Locate and identify every blood parasite.
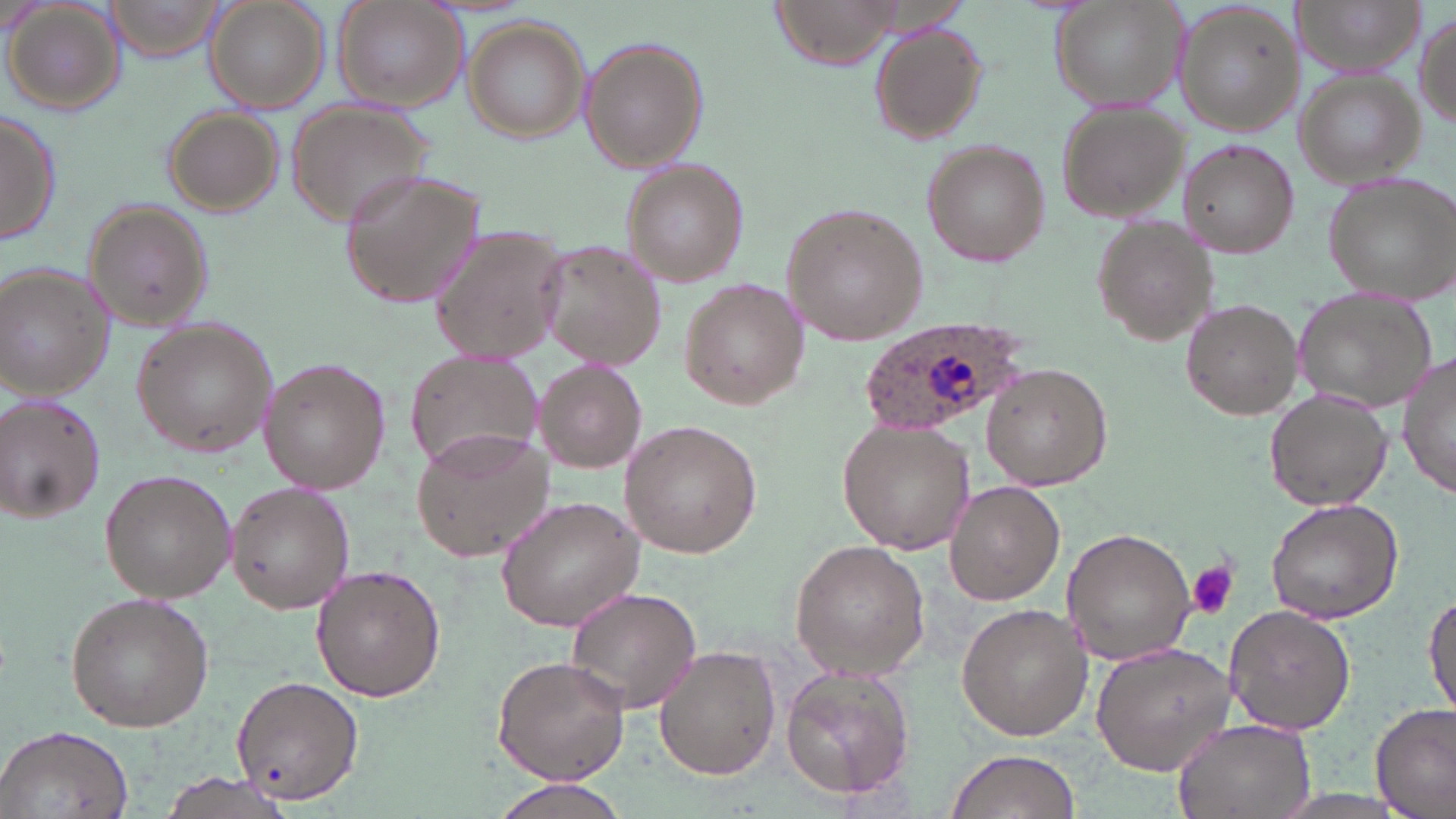

Approximate bounding boxes as (x1,y1)-(x2,y2) corner pairs in pixels.
Plasmodium ovale-infected red blood cells: (865,320)-(1031,440).
No Plasmodium falciparum, Plasmodium malariae, Plasmodium vivax, Babesia divergens, or Trypanosoma brucei observed.

Uninfected red blood cell locations: (202,0)-(332,113), (333,0)-(466,112), (770,0)-(908,71), (1051,0)-(1190,112), (1298,0)-(1421,73), (1174,2)-(1303,139), (4,4)-(125,114), (1414,11)-(1455,133), (464,17)-(590,145), (868,22)-(987,145), (581,36)-(708,175), (1294,70)-(1426,188), (288,102)-(433,229), (1056,104)-(1189,223), (161,107)-(286,219), (0,109)-(61,246), (923,141)-(1050,267), (1179,141)-(1299,258), (622,161)-(747,284), (340,168)-(486,312), (1323,173)-(1456,305), (86,204)-(215,332), (783,205)-(928,345), (1091,216)-(1215,349), (429,223)-(572,365), (539,243)-(668,370), (1,264)-(114,401), (679,279)-(807,409), (1296,290)-(1437,414), (1183,299)-(1304,420), (131,318)-(279,457), (1398,345)-(1455,502), (405,356)-(545,479), (259,359)-(390,495), (535,359)-(648,472), (983,363)-(1111,489), (1265,389)-(1394,511), (0,394)-(107,524), (622,420)-(763,556), (839,420)-(974,552), (412,425)-(555,562), (100,468)-(237,603), (225,480)-(354,614), (943,480)-(1065,607), (497,495)-(648,630), (1265,498)-(1407,624), (1062,527)-(1199,664), (790,539)-(930,680), (310,565)-(445,701), (565,586)-(701,716), (1424,587)-(1456,718), (64,591)-(215,732), (956,604)-(1093,741), (1223,605)-(1356,735), (1089,640)-(1237,776), (654,645)-(781,780), (492,655)-(630,785), (779,665)-(917,799), (229,676)-(366,807), (1372,704)-(1455,819), (1171,717)-(1316,819), (0,723)-(135,819), (943,748)-(1081,819), (158,773)-(298,818), (489,776)-(634,819). Platelet locations: (1187,562)-(1238,619). Slide-level diagnosis: Plasmodium ovale. One field of a larger specimen. Light microscopy. May-Grünwald-Giemsa stain. Image is 1456×819 pixels. Thin blood smear. 1000x magnification.